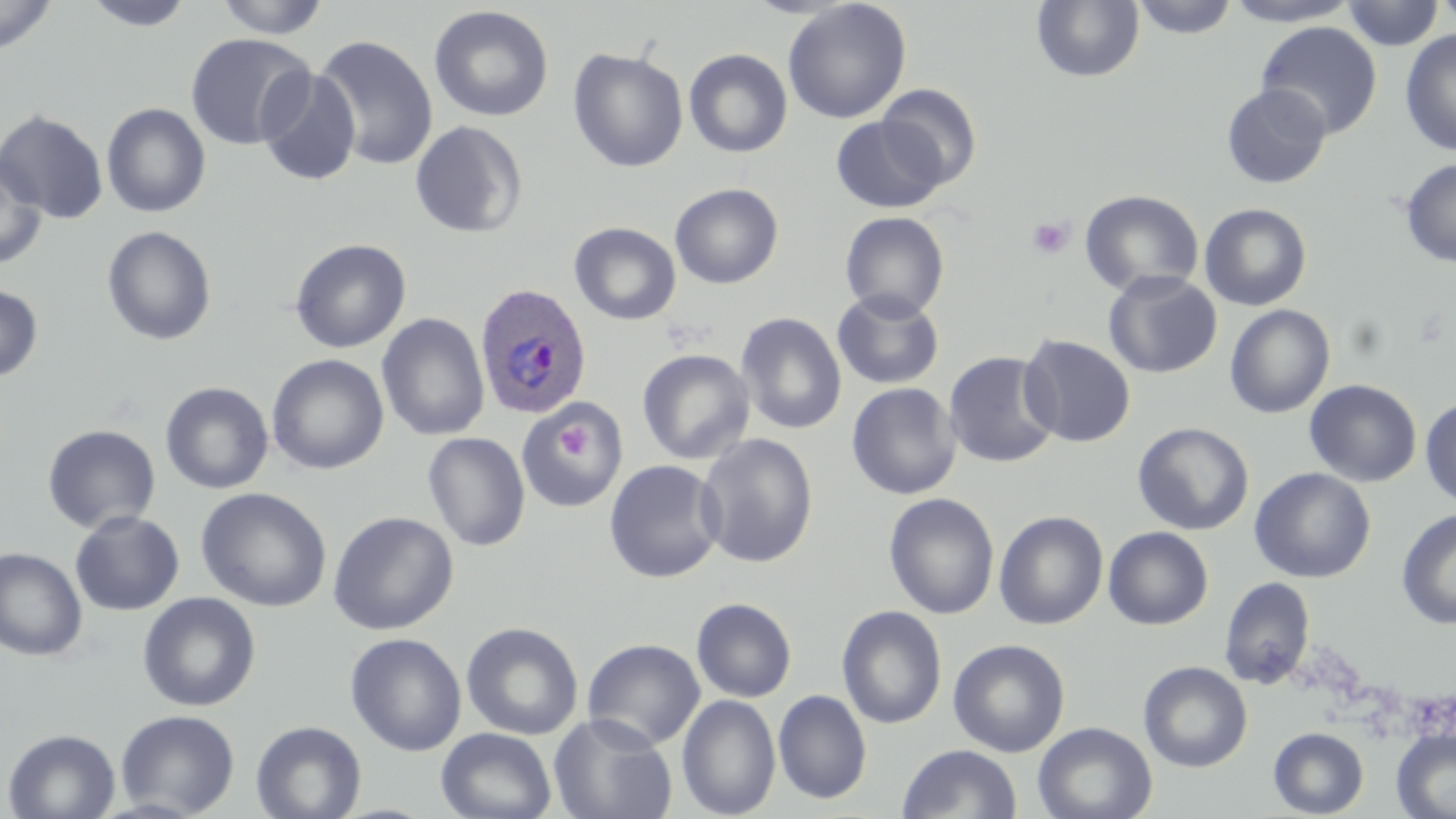
Approximate bounding boxes as (x1,y1)-(x2,y2) corner pairs in pixels. Plasmodium ovale-infected red blood cell locations: (474,283)-(592,419). Platelet locations: (1026,215)-(1075,260), (659,315)-(710,352), (550,420)-(596,470). Uninfected red blood cell locations: (0,0)-(57,56), (214,0)-(330,39), (1131,0)-(1239,40), (1222,0)-(1362,26), (1435,0)-(1456,29), (84,1)-(195,31), (783,1)-(911,124), (1030,1)-(1145,84), (1341,1)-(1444,50), (428,5)-(554,123), (1255,21)-(1382,139), (1400,29)-(1456,156), (184,33)-(316,151), (312,34)-(438,171), (567,48)-(688,172), (684,48)-(793,158), (257,68)-(362,187), (1221,83)-(1331,188), (876,84)-(981,189), (101,103)-(211,217), (0,109)-(109,223), (830,115)-(945,214), (410,120)-(528,238), (0,154)-(48,268), (1399,158)-(1456,268), (669,183)-(784,289), (1079,189)-(1204,298), (1198,203)-(1312,311), (840,211)-(949,320), (569,222)-(681,325), (101,225)-(217,346), (289,238)-(411,354), (1103,271)-(1222,379), (0,284)-(43,381), (831,289)-(945,390), (1225,305)-(1335,418), (735,312)-(847,435), (376,313)-(490,441), (1018,334)-(1136,447), (636,348)-(755,465), (943,351)-(1060,469), (266,354)-(389,475), (1304,379)-(1422,487), (159,381)-(274,494), (846,382)-(961,500), (1420,396)-(1456,509), (517,401)-(629,512), (1133,422)-(1254,535), (42,424)-(161,534), (423,431)-(531,552), (696,433)-(819,568), (604,459)-(725,583), (1249,467)-(1376,583), (195,487)-(332,612), (883,492)-(1000,619), (1396,508)-(1456,630), (69,510)-(184,616), (993,510)-(1109,630), (327,511)-(459,635), (1103,526)-(1213,630), (0,547)-(88,661), (1218,577)-(1315,690), (137,592)-(260,712), (691,597)-(797,702), (836,605)-(947,729), (461,621)-(584,741), (345,632)-(467,756), (582,638)-(705,750), (948,639)-(1070,757), (1138,661)-(1252,772), (773,689)-(872,805), (677,694)-(781,818), (115,709)-(240,817), (548,713)-(677,819), (250,720)-(366,819), (1032,721)-(1157,819), (1268,727)-(1368,817), (2,728)-(121,818), (436,728)-(557,819), (1391,728)-(1456,818), (897,744)-(1023,818). Slide-level diagnosis: Plasmodium ovale. Image is 1456×819 pixels. Single field of view. Captured at 1000x magnification. Thin blood smear. Light microscopy. May-Grünwald-Giemsa-stained preparation.